Report the malaria status of this cell.
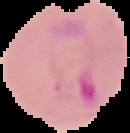

It is parasitized.

image size = 130×133 pixels
image type = segmented cell region on a black background
preparation = thin blood film